Assess the morphology of the erythrocytes.
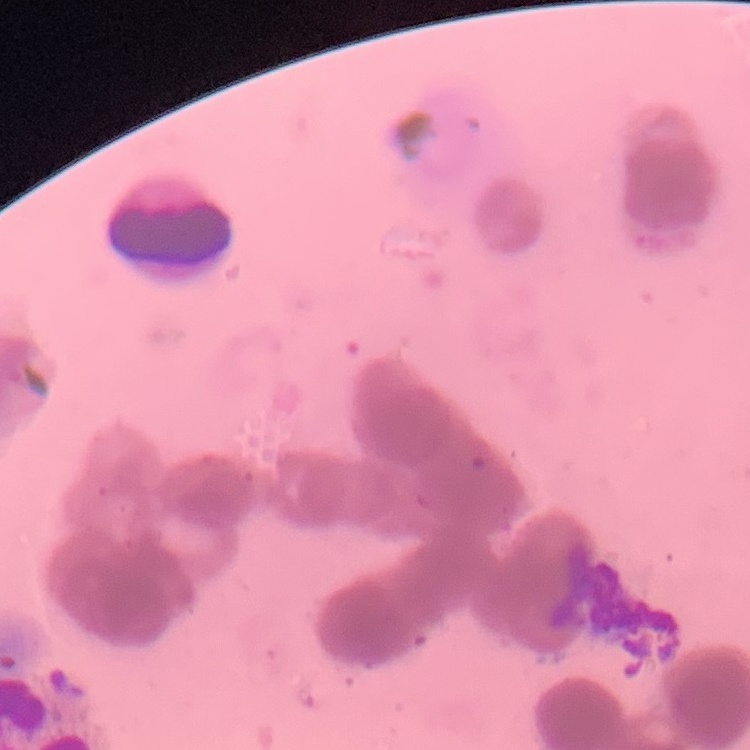
They show rouleaux formation.

Thin blood film. Square crop of a larger photomicrograph. Field's or Giemsa stain.